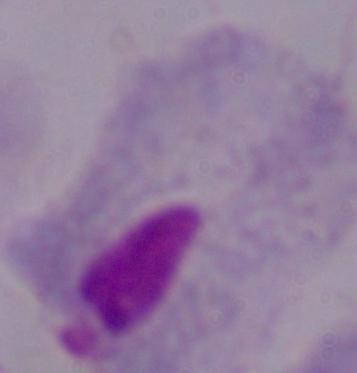
Summary:
  - Magnification: 1000x
  - Identification: trichomonad
  - Modality: micrograph